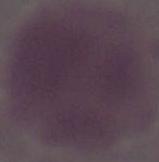

Photomicrograph. Captured at 1000x magnification. A red blood cell is shown.